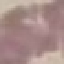
malaria status = uninfected
stain = Giemsa
preparation = thin blood film
image type = automatically extracted cell patch, resized to 64 × 64 pixels
capture = smartphone camera at the microscope eyepiece